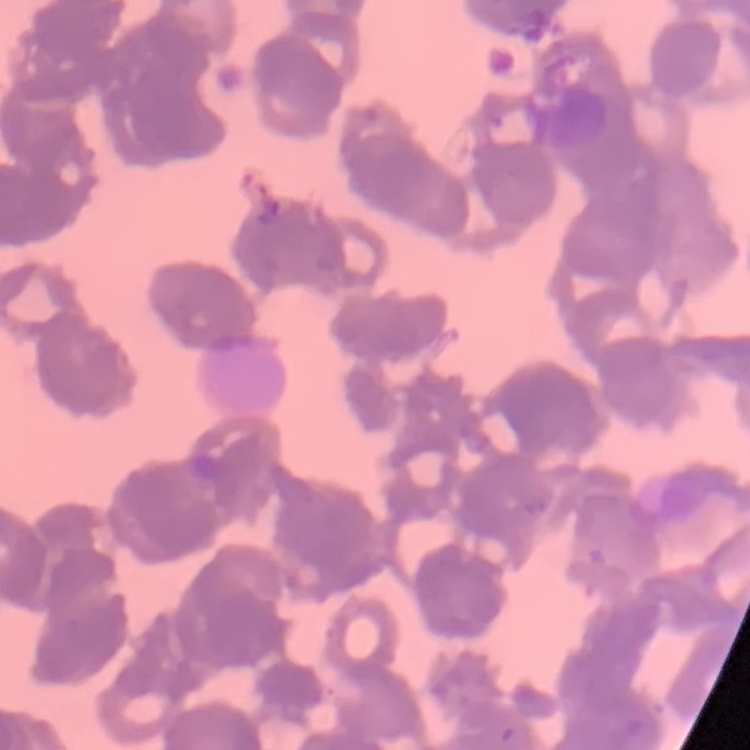
Summary:
  - Red blood cell morphology: rouleaux formation
  - Image type: one tile cut from a larger photomicrograph
  - Stain: Field's or Giemsa
  - Preparation: thin peripheral smear